Assess this cell for malaria.
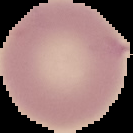
It is uninfected.

Summary:
  - Preparation: thin blood film
  - Image size: 133×133 pixels
  - Image type: cell region segmented out of the field of view; surrounding area masked to black